Report the malaria status of this cell.
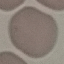

It is uninfected.

Giemsa-stained preparation. Cell patch, automatically extracted from a larger field of view and resized to 64 × 64 pixels. Acquired by smartphone through the microscope eyepiece. Thin blood smear.